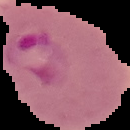 The area outside the segmented cell region is set to black. Result: Plasmodium parasites identified. From a thin blood smear. Image is 130×130 pixels.